Report the malaria status of this cell.
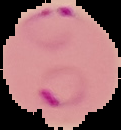

It is parasitized.

From a thin blood smear. Image is 121×130 pixels. The area outside the segmented cell region is set to black.